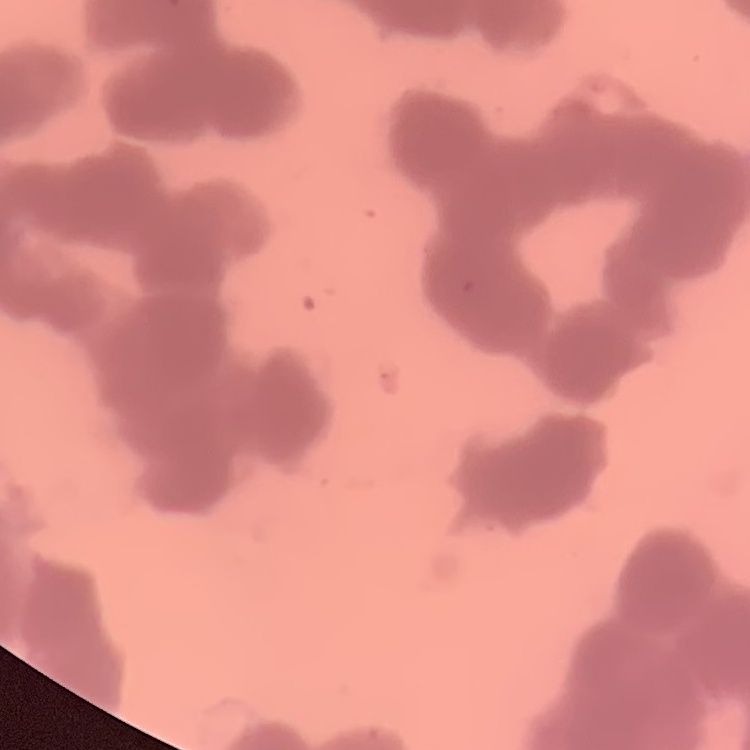
red blood cell morphology = rouleaux formation
stain = Field's or Giemsa
image type = one tile cut from a larger photomicrograph
preparation = thin blood smear